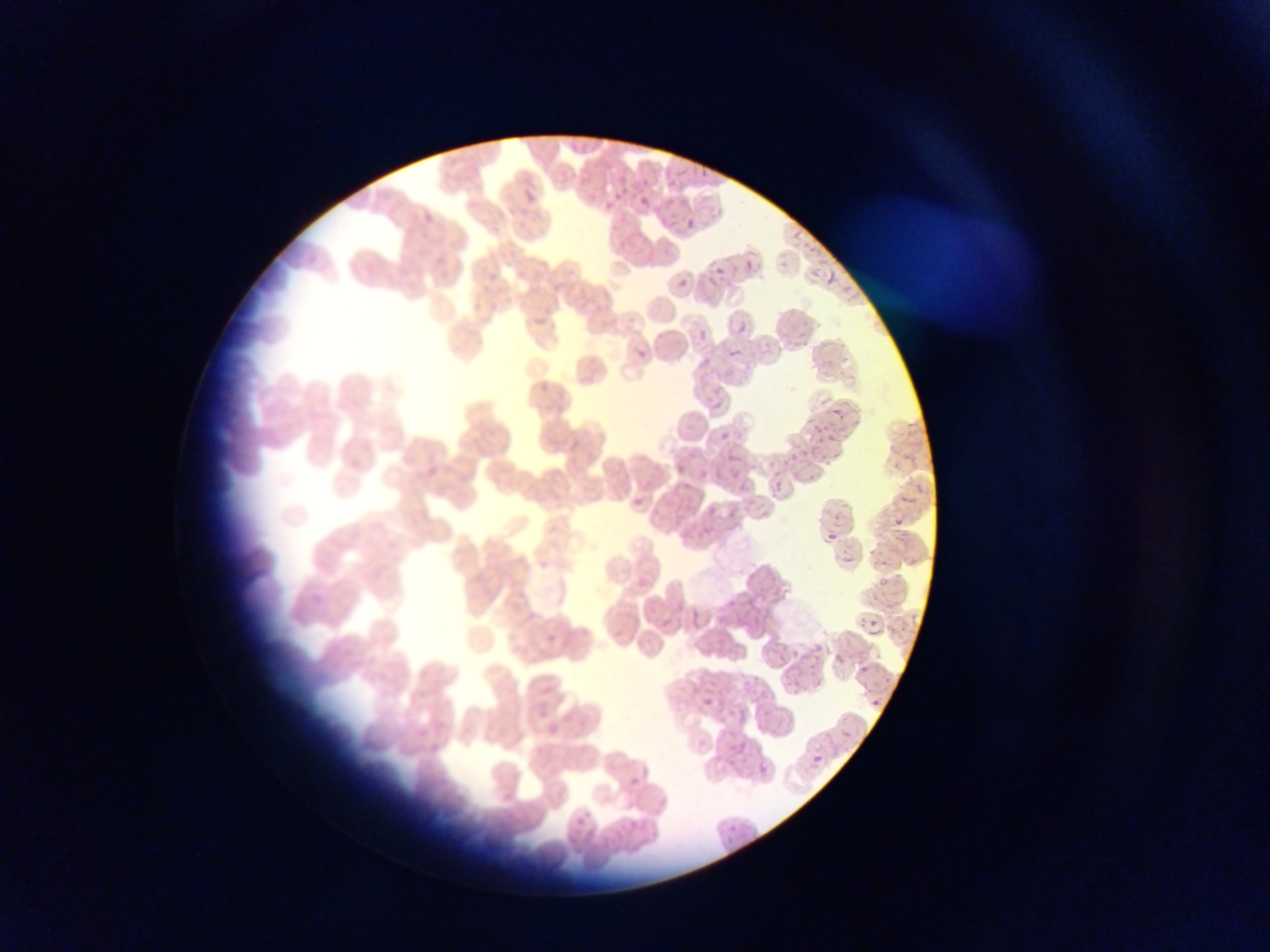

Approximate bounding boxes as [left, top, right, bottom] in pixels. Malaria parasite locations: [666, 181, 677, 191], [523, 190, 536, 203], [640, 197, 651, 207], [686, 219, 696, 228], [791, 230, 801, 242], [743, 260, 758, 273], [746, 262, 756, 271], [715, 269, 724, 277], [827, 270, 835, 289], [679, 279, 688, 288], [738, 324, 748, 334], [699, 331, 707, 340], [636, 350, 646, 359], [730, 350, 738, 358], [828, 410, 843, 422], [719, 432, 729, 442], [728, 453, 738, 463], [676, 465, 685, 475], [633, 498, 642, 508], [708, 507, 719, 516], [825, 511, 844, 524], [895, 519, 904, 527], [828, 533, 837, 542], [843, 558, 854, 564], [880, 560, 889, 569], [880, 579, 889, 589], [866, 622, 878, 629], [859, 665, 869, 675], [813, 681, 823, 690], [872, 695, 880, 707], [703, 699, 714, 708], [873, 700, 883, 707], [733, 740, 749, 755], [811, 754, 824, 766], [628, 777, 642, 789]. Thin blood smear. One field of view. Photographed through a microscope with a mobile-phone camera. Sample from Ghana. Image is 1270×952 pixels.